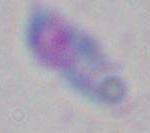
Summary:
  - Modality: photomicrograph
  - Magnification: 1000x
  - Identification: Toxoplasma gondii